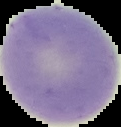
Image is 121×127 pixels. From a thin blood smear. Cell region segmented out of the field of view; the surrounding area is masked to black. Result: no malaria parasites detected.